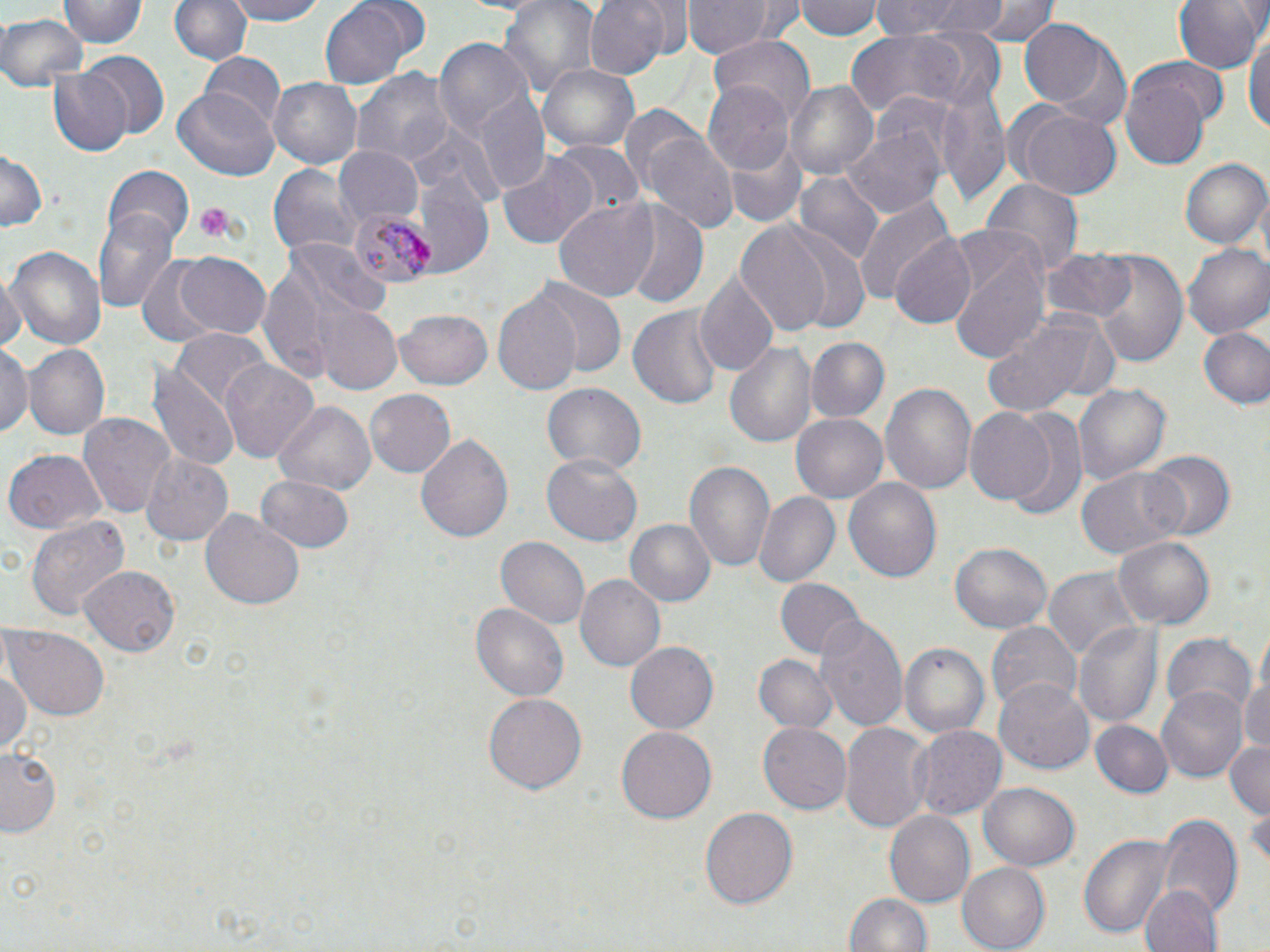 Approximate bounding boxes as (x1, y1, x2, y2) in pixels. Uninfected red blood cell locations: (61, 0, 144, 49), (171, 0, 250, 66), (222, 0, 334, 25), (498, 0, 600, 102), (582, 0, 673, 80), (682, 0, 781, 60), (797, 0, 882, 40), (870, 0, 980, 39), (969, 0, 1058, 43), (1174, 0, 1265, 74), (320, 1, 416, 88), (0, 13, 86, 91), (1019, 17, 1128, 130), (1244, 26, 1270, 141), (844, 30, 980, 115), (710, 35, 816, 120), (433, 38, 532, 139), (75, 52, 169, 146), (201, 52, 286, 134), (540, 65, 639, 154), (47, 68, 131, 155), (354, 69, 454, 169), (1121, 71, 1212, 175), (267, 77, 363, 170), (705, 82, 796, 173), (786, 82, 878, 181), (175, 87, 279, 181), (469, 89, 547, 194), (939, 89, 1011, 206), (618, 104, 703, 196), (1009, 105, 1122, 198), (843, 124, 947, 218), (407, 126, 502, 211), (643, 132, 739, 236), (725, 137, 806, 229), (550, 141, 643, 221), (332, 146, 423, 226), (0, 149, 46, 234), (495, 153, 599, 251), (1178, 158, 1267, 249), (411, 159, 495, 274), (267, 162, 359, 259), (103, 164, 193, 249), (794, 171, 884, 267), (980, 181, 1082, 281), (854, 194, 954, 306), (551, 198, 659, 303), (622, 203, 709, 307), (93, 210, 179, 314), (736, 222, 835, 339), (944, 231, 1050, 365), (888, 234, 977, 331), (284, 240, 388, 321), (5, 244, 105, 354), (1183, 245, 1270, 340), (1041, 247, 1137, 322), (1085, 249, 1188, 367), (174, 252, 272, 340), (134, 259, 223, 342), (696, 272, 780, 378), (0, 276, 22, 356), (530, 280, 628, 382), (493, 292, 583, 398), (314, 304, 402, 395), (627, 305, 724, 413), (394, 308, 495, 390), (979, 309, 1119, 420), (1200, 327, 1270, 408), (171, 331, 271, 414), (804, 335, 890, 422), (722, 340, 819, 451), (0, 344, 31, 439), (24, 344, 110, 440), (220, 358, 319, 463), (149, 363, 241, 472), (541, 381, 645, 476), (1073, 381, 1170, 486), (880, 382, 978, 499), (364, 388, 455, 479), (271, 397, 377, 495), (964, 407, 1057, 507), (998, 408, 1089, 520), (78, 412, 176, 518), (789, 412, 887, 505), (417, 432, 514, 546), (4, 449, 107, 534), (1140, 451, 1235, 543), (138, 452, 234, 546), (544, 454, 641, 545), (686, 460, 777, 574), (1077, 466, 1190, 560), (258, 473, 355, 553), (845, 477, 943, 581), (752, 491, 840, 587), (201, 506, 306, 610), (25, 513, 130, 620), (625, 518, 715, 608), (1115, 535, 1216, 633), (496, 536, 591, 632), (951, 544, 1051, 633), (79, 566, 181, 656), (1042, 567, 1140, 665), (577, 574, 666, 673), (774, 576, 862, 659), (470, 601, 569, 703), (816, 613, 911, 735), (1074, 619, 1166, 731), (987, 620, 1082, 716), (3, 627, 109, 719), (1163, 634, 1257, 721), (627, 642, 719, 732), (898, 643, 989, 738), (754, 655, 839, 733), (0, 665, 30, 756), (1241, 668, 1270, 756), (994, 679, 1095, 775), (1154, 686, 1247, 783), (483, 693, 585, 795), (757, 721, 851, 816), (840, 721, 933, 831), (1092, 721, 1174, 799), (912, 725, 1007, 822), (617, 727, 716, 820), (1226, 740, 1270, 818), (1, 749, 63, 835), (980, 782, 1080, 871), (700, 807, 799, 911), (881, 810, 976, 910), (1157, 816, 1242, 922), (1078, 831, 1177, 937), (957, 861, 1052, 952), (1140, 883, 1222, 952), (846, 890, 933, 952). Platelet locations: (191, 202, 239, 243). Plasmodium malariae-infected red blood cell locations: (347, 207, 435, 287). Slide-level diagnosis: Plasmodium malariae. Thin blood smear. May-Grünwald-Giemsa-stained preparation. Optical microscopy. Single field of view. Image is 1270×952 pixels. 1000x magnification.